State which cell type is depicted.
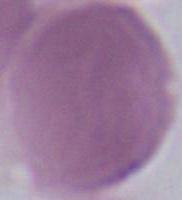

This is an erythrocyte.

Micrograph. Captured at 1000x magnification.